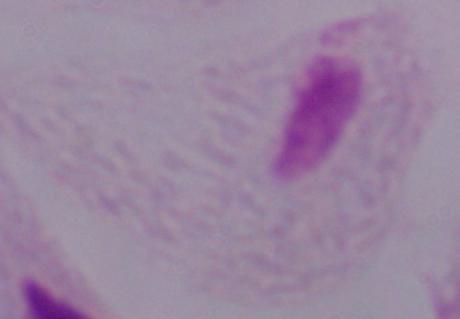
{
  "modality": "photomicrograph",
  "magnification": "1000x",
  "identification": "trichomonad"
}